Classify this cell by malaria status.
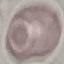
Uninfected.

Summary:
  - Capture: smartphone camera at the microscope eyepiece
  - Preparation: thin smear
  - Image type: automatically extracted cell patch, resized to 64 × 64 pixels
  - Stain: Giemsa